Give a bounding box for every malaria parasite, every leukocyte, and every artifact (stain precipitate or debris).
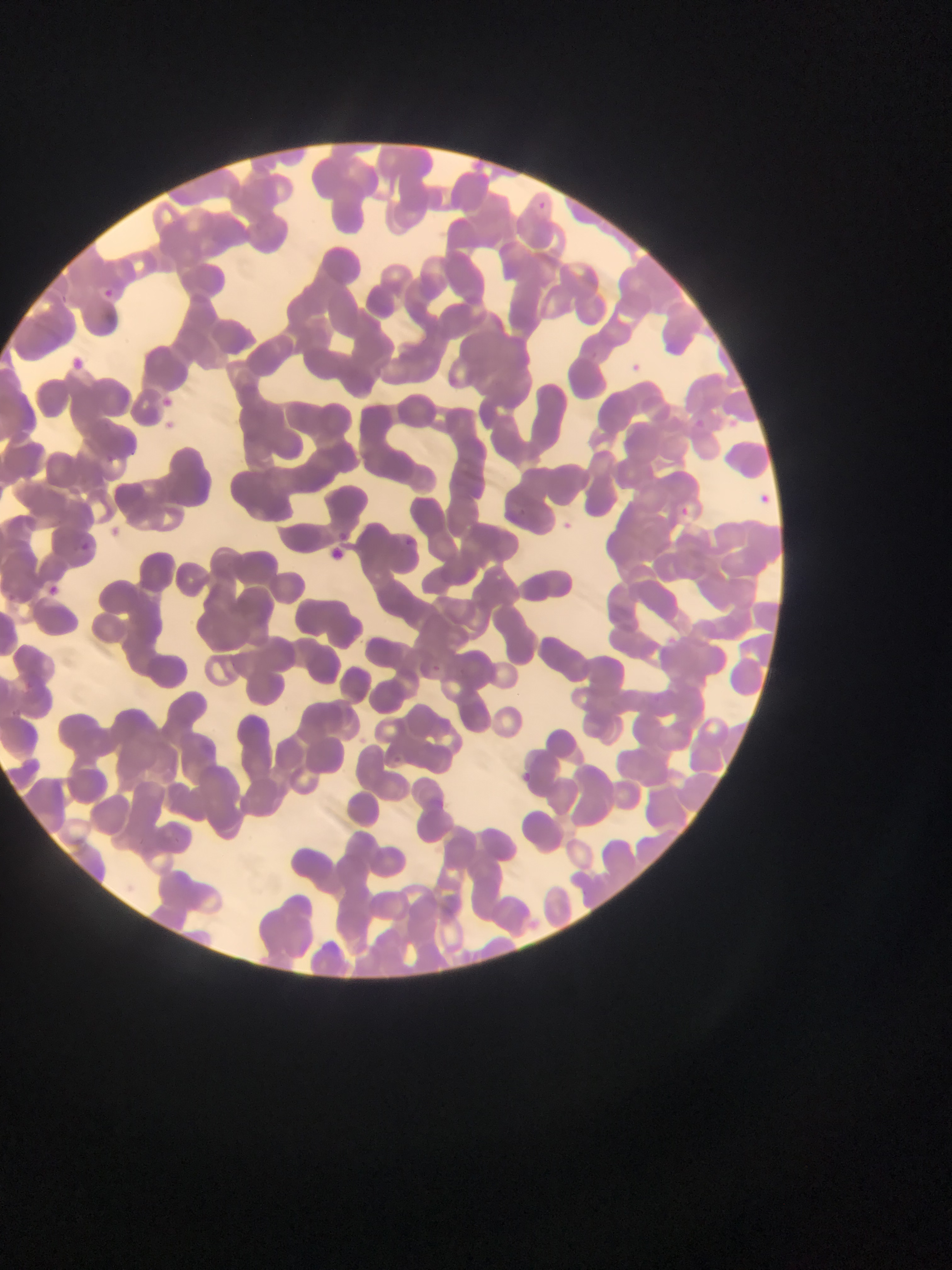

Approximate bounding boxes as [left, top, right, bottom] in pixels.
Malaria parasites: [526, 190, 551, 220], [98, 282, 115, 298], [68, 352, 91, 369], [628, 359, 646, 373], [155, 390, 178, 415], [727, 413, 745, 430], [690, 414, 706, 430], [162, 416, 180, 434], [125, 441, 142, 460], [104, 446, 116, 460], [759, 488, 768, 515], [678, 503, 691, 520], [561, 514, 581, 539], [328, 523, 344, 548], [404, 530, 413, 548], [76, 537, 96, 555], [46, 581, 66, 604], [432, 657, 442, 675], [389, 752, 404, 764], [520, 767, 536, 785].
No leukocytes observed.

country = Ghana
capture = mobile-phone photograph through a microscope
image size = 952×1270 pixels
preparation = thin blood film
field of view = single